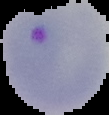
image type = segmented cell region with the area outside set to black
image size = 109×115 pixels
malaria status = parasitized
preparation = thin blood smear